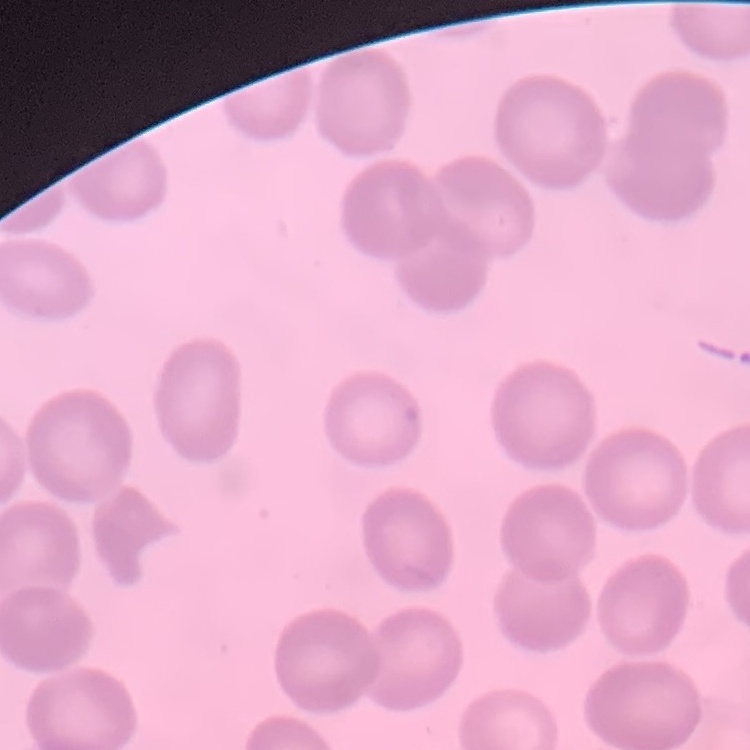
{
  "red_blood_cell_morphology": "no rouleaux formation",
  "stain": "Field's or Giemsa",
  "image_type": "square crop of a larger photomicrograph",
  "preparation": "thin blood smear"
}